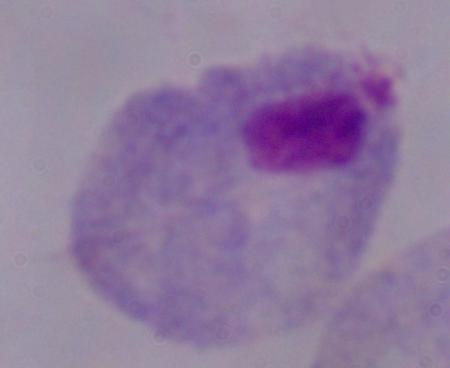

Summary:
  - Identification: trichomonad
  - Magnification: 1000x
  - Modality: micrograph